State the preparation type.
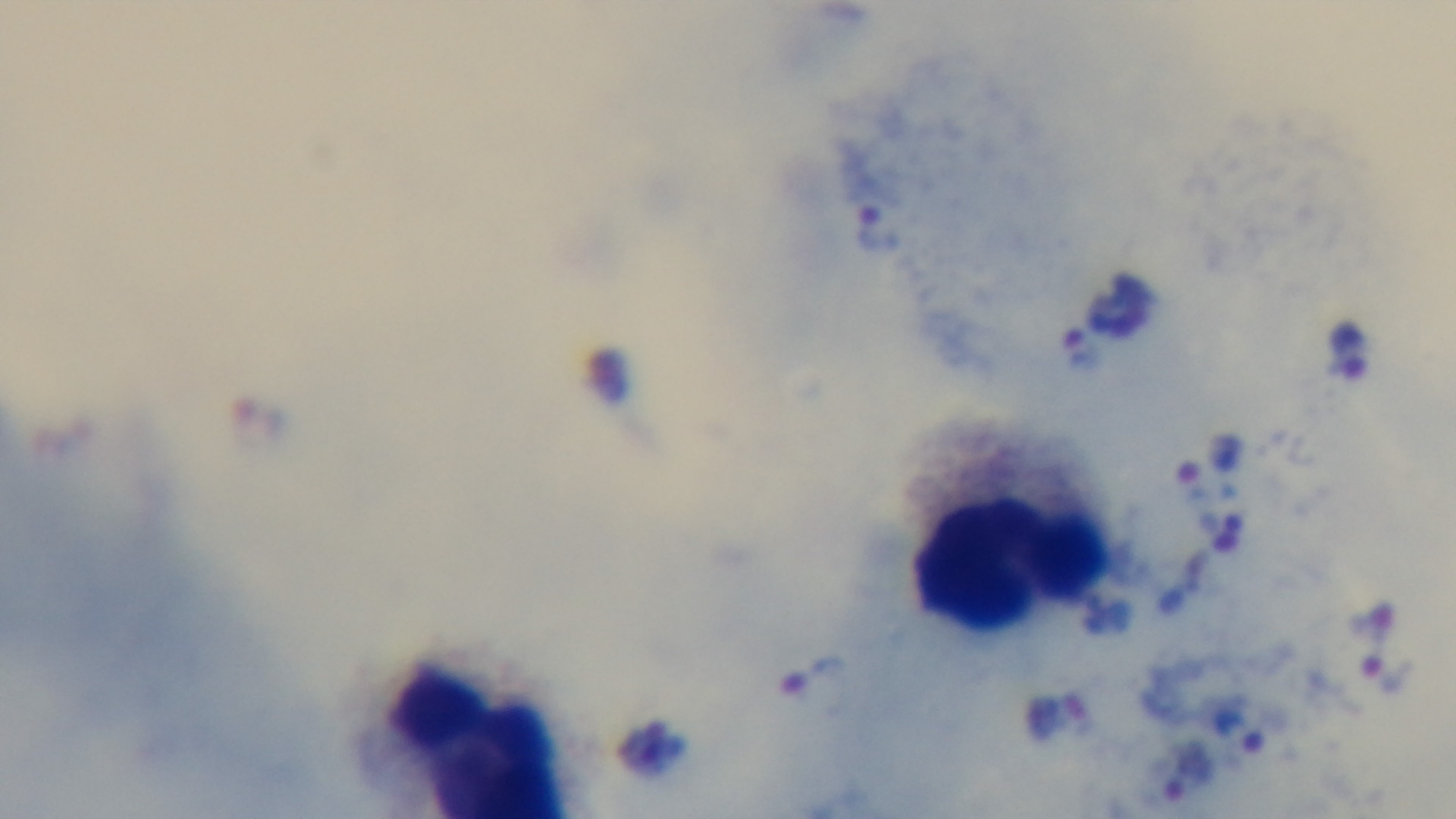

It is a thick blood film.

Summary:
  - Objective: 100x oil immersion
  - Field of view: one from the slide
  - Malaria status: infected
  - Stain: Giemsa
  - Capture: mounted 4K digital camera
  - Modality: light microscopy